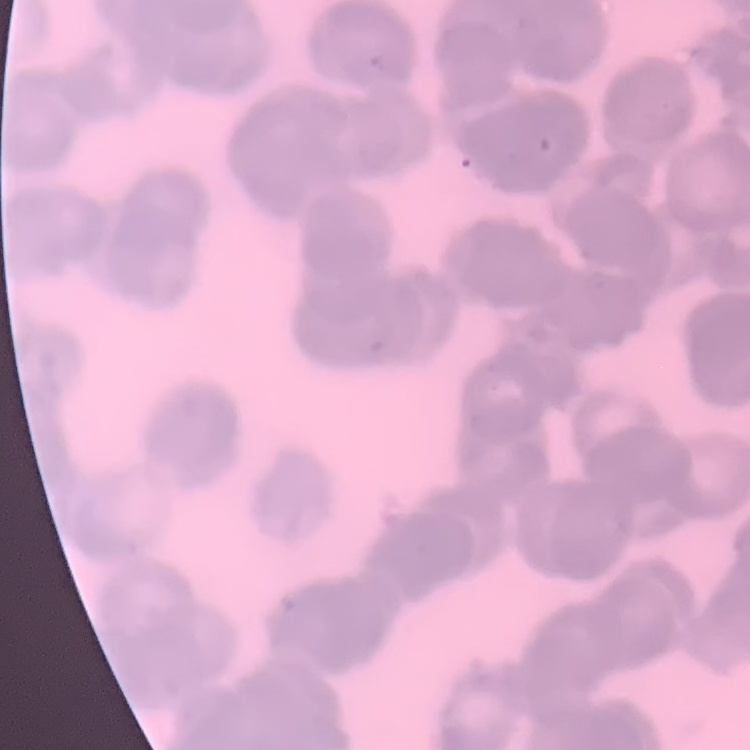

erythrocyte morphology = rouleaux formation
stain = Field's or Giemsa
preparation = thin blood film
image type = one tile cut from a larger photomicrograph